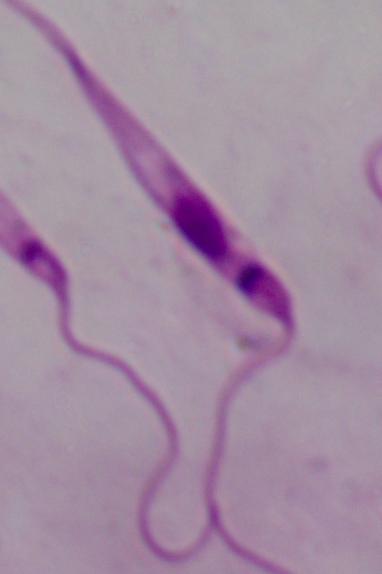

Captured at 1000x magnification. Photomicrograph. A Leishmania parasite is shown.